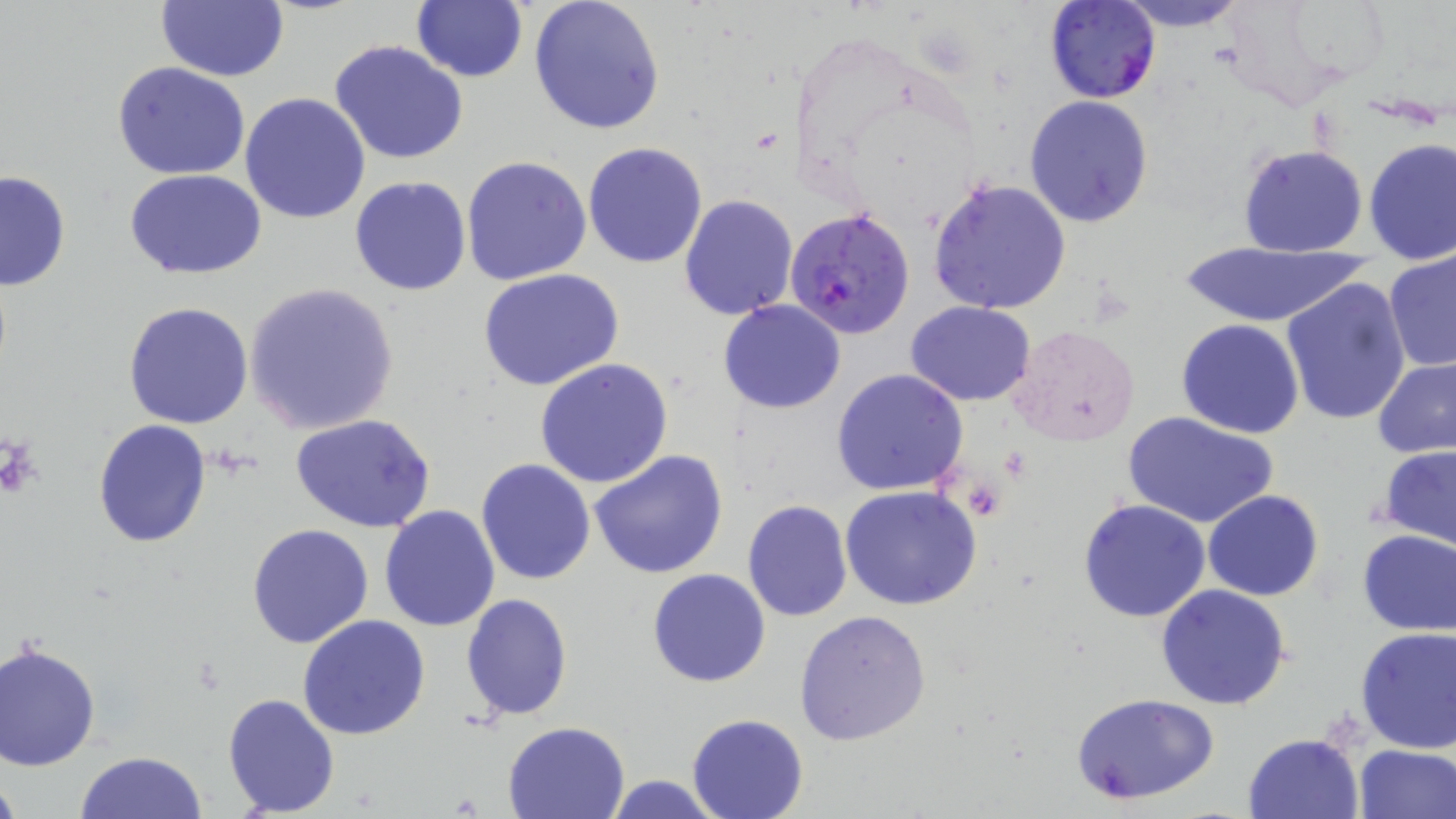
Approximate bounding boxes as named x1/y1/x2/y2 corners in pixels. Platelet locations: (x1=3, y1=437, x2=43, y2=495). Uninfected red blood cell locations: (x1=158, y1=0, x2=290, y2=82), (x1=411, y1=0, x2=526, y2=82), (x1=529, y1=0, x2=665, y2=136), (x1=1112, y1=0, x2=1250, y2=30), (x1=329, y1=41, x2=468, y2=165), (x1=113, y1=61, x2=251, y2=180), (x1=240, y1=92, x2=372, y2=225), (x1=1024, y1=96, x2=1153, y2=228), (x1=1362, y1=138, x2=1455, y2=264), (x1=583, y1=142, x2=708, y2=267), (x1=1237, y1=144, x2=1369, y2=258), (x1=461, y1=155, x2=592, y2=286), (x1=124, y1=169, x2=267, y2=278), (x1=0, y1=170, x2=73, y2=291), (x1=350, y1=175, x2=472, y2=296), (x1=927, y1=176, x2=1072, y2=315), (x1=679, y1=193, x2=798, y2=320), (x1=1181, y1=242, x2=1368, y2=329), (x1=1384, y1=252, x2=1456, y2=374), (x1=479, y1=269, x2=625, y2=392), (x1=1280, y1=276, x2=1413, y2=427), (x1=244, y1=282, x2=400, y2=435), (x1=719, y1=299, x2=846, y2=414), (x1=122, y1=301, x2=254, y2=430), (x1=905, y1=301, x2=1035, y2=405), (x1=1176, y1=319, x2=1306, y2=438), (x1=1007, y1=322, x2=1138, y2=447), (x1=1373, y1=357, x2=1456, y2=459), (x1=534, y1=358, x2=674, y2=489), (x1=830, y1=369, x2=969, y2=496), (x1=1123, y1=411, x2=1281, y2=530), (x1=292, y1=414, x2=439, y2=533), (x1=93, y1=420, x2=211, y2=549), (x1=1377, y1=444, x2=1456, y2=553), (x1=589, y1=448, x2=730, y2=579), (x1=476, y1=459, x2=596, y2=587), (x1=840, y1=486, x2=985, y2=611), (x1=1203, y1=490, x2=1324, y2=602), (x1=1079, y1=498, x2=1212, y2=623), (x1=741, y1=499, x2=852, y2=621), (x1=379, y1=504, x2=501, y2=631), (x1=247, y1=522, x2=375, y2=648), (x1=1356, y1=528, x2=1456, y2=635), (x1=647, y1=568, x2=771, y2=687), (x1=1155, y1=584, x2=1293, y2=710), (x1=461, y1=593, x2=573, y2=720), (x1=794, y1=609, x2=931, y2=744), (x1=297, y1=615, x2=430, y2=740), (x1=1355, y1=626, x2=1456, y2=752), (x1=0, y1=641, x2=101, y2=771), (x1=223, y1=692, x2=340, y2=815), (x1=1073, y1=692, x2=1219, y2=806), (x1=687, y1=714, x2=810, y2=819), (x1=502, y1=720, x2=629, y2=819), (x1=1244, y1=734, x2=1364, y2=819), (x1=1353, y1=743, x2=1455, y2=819), (x1=73, y1=751, x2=208, y2=819), (x1=0, y1=774, x2=21, y2=819), (x1=603, y1=775, x2=726, y2=817). Plasmodium falciparum-infected red blood cell locations: (x1=1045, y1=0, x2=1160, y2=104), (x1=785, y1=207, x2=915, y2=339). Slide-level diagnosis: Plasmodium falciparum. Thin blood film. Light microscopy. Captured at 1000x magnification. Image is 1456×819 pixels. May-Grünwald-Giemsa stain. One field of a larger specimen.